Outline every leukocyte.
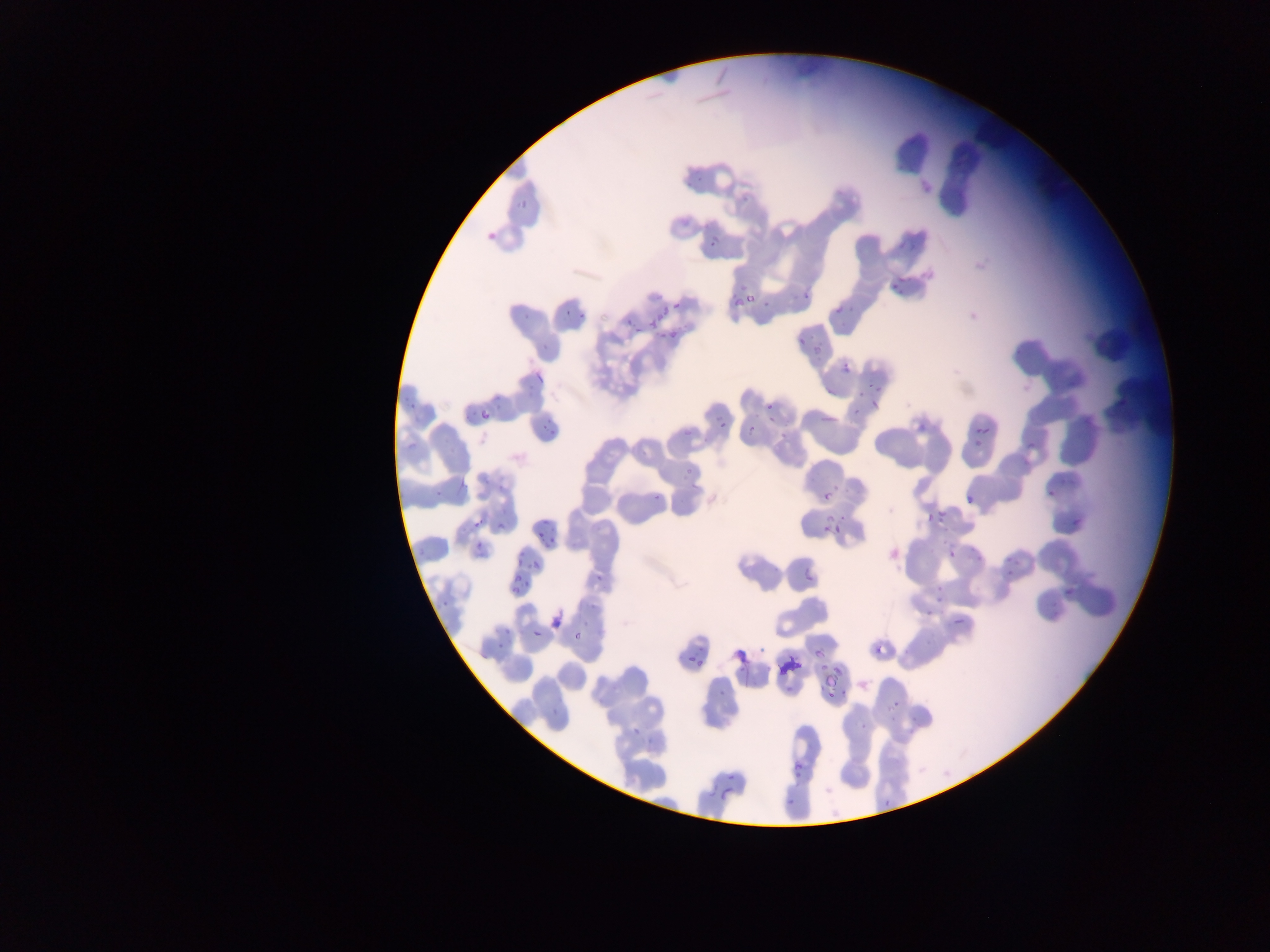
No leukocytes observed.

Approximate bounding boxes as [left, top, right, bottom] in pixels.
Summary:
  - Plasmodium parasite locations: [684, 170, 701, 190], [741, 189, 758, 206], [513, 197, 528, 210], [483, 226, 498, 243], [897, 232, 929, 252], [711, 237, 720, 247], [887, 279, 914, 295], [795, 283, 816, 298], [744, 290, 755, 305], [756, 293, 776, 308], [834, 295, 854, 311], [731, 297, 743, 307], [673, 302, 682, 310], [834, 304, 858, 332], [561, 306, 574, 322], [576, 306, 593, 322], [520, 310, 533, 322], [645, 310, 671, 327], [627, 322, 645, 335], [666, 324, 686, 343], [797, 335, 805, 344], [808, 337, 829, 356], [539, 343, 548, 350], [841, 363, 851, 374], [533, 372, 544, 383], [1065, 379, 1076, 390], [860, 381, 887, 400], [1118, 388, 1132, 410], [411, 390, 424, 414], [483, 390, 506, 411], [869, 393, 884, 412], [853, 399, 863, 421], [766, 403, 775, 412], [478, 409, 490, 421], [463, 410, 472, 417], [821, 413, 834, 425], [917, 419, 932, 432], [974, 419, 996, 434], [541, 420, 560, 435], [677, 420, 694, 447], [717, 420, 726, 429], [747, 422, 762, 434], [771, 427, 793, 444], [407, 435, 418, 452], [973, 435, 985, 450], [1025, 437, 1042, 454], [681, 461, 695, 476], [458, 472, 466, 494], [1057, 474, 1078, 494], [828, 479, 849, 494], [434, 481, 446, 503], [1041, 486, 1058, 500], [958, 491, 977, 509], [822, 492, 832, 502], [654, 498, 665, 508], [933, 505, 948, 523], [925, 511, 942, 523], [495, 513, 510, 530], [537, 516, 556, 542], [473, 518, 485, 530], [1070, 518, 1083, 532], [834, 522, 842, 532], [422, 534, 431, 548], [513, 537, 533, 565], [475, 540, 490, 553], [966, 543, 981, 560], [949, 549, 957, 559], [1005, 554, 1017, 566], [529, 559, 539, 570], [597, 562, 610, 579], [997, 566, 1018, 585], [805, 573, 814, 583], [509, 574, 527, 585], [511, 585, 521, 594], [1062, 586, 1075, 598], [933, 587, 947, 604], [438, 598, 459, 615], [1049, 599, 1064, 619], [549, 605, 569, 631], [921, 610, 934, 620], [952, 614, 967, 628], [532, 629, 541, 638], [573, 631, 581, 640], [495, 632, 510, 653], [735, 632, 758, 666], [923, 639, 936, 650], [871, 640, 886, 660], [693, 642, 706, 653], [758, 644, 771, 655], [901, 645, 908, 660], [813, 648, 822, 656], [694, 659, 703, 668], [792, 659, 802, 669], [816, 661, 831, 680], [776, 665, 786, 675], [831, 669, 851, 681], [786, 679, 794, 694], [824, 681, 841, 706], [715, 687, 728, 707], [886, 695, 899, 712], [550, 700, 555, 718], [631, 715, 646, 739], [850, 722, 871, 733], [905, 724, 919, 744], [641, 736, 655, 750], [786, 743, 802, 775], [727, 773, 738, 782], [721, 789, 730, 800], [786, 794, 799, 815], [882, 796, 894, 799] | approximate [x, y] pixel centers of objects too small to bound: [822, 533]
  - Capture: mobile-phone photograph through a microscope
  - Preparation: thin blood smear
  - Field of view: single
  - Country: Ghana
  - Image size: 1270×952 pixels